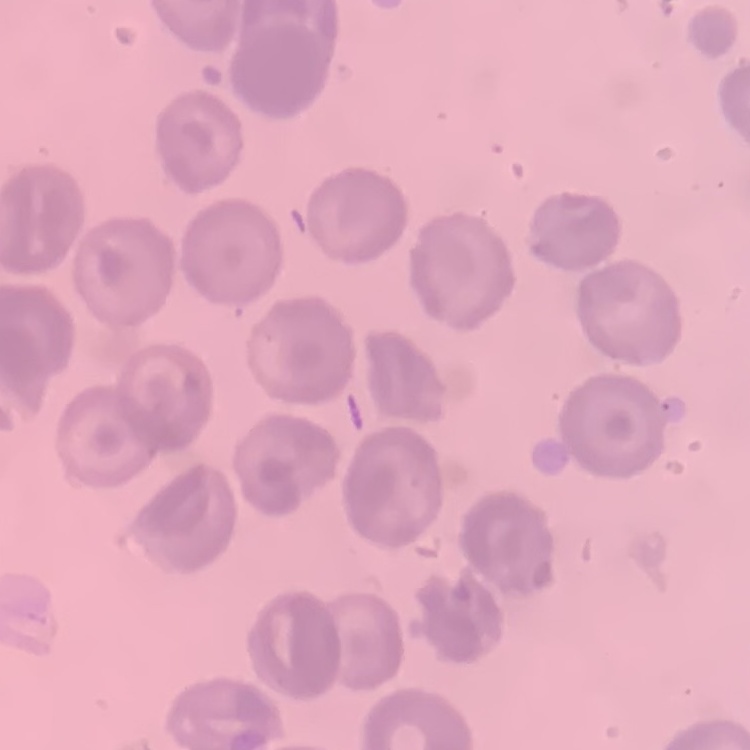
erythrocyte morphology = no rouleaux formation
preparation = thin peripheral smear
image type = square crop of a larger photomicrograph
stain = Field's or Giemsa